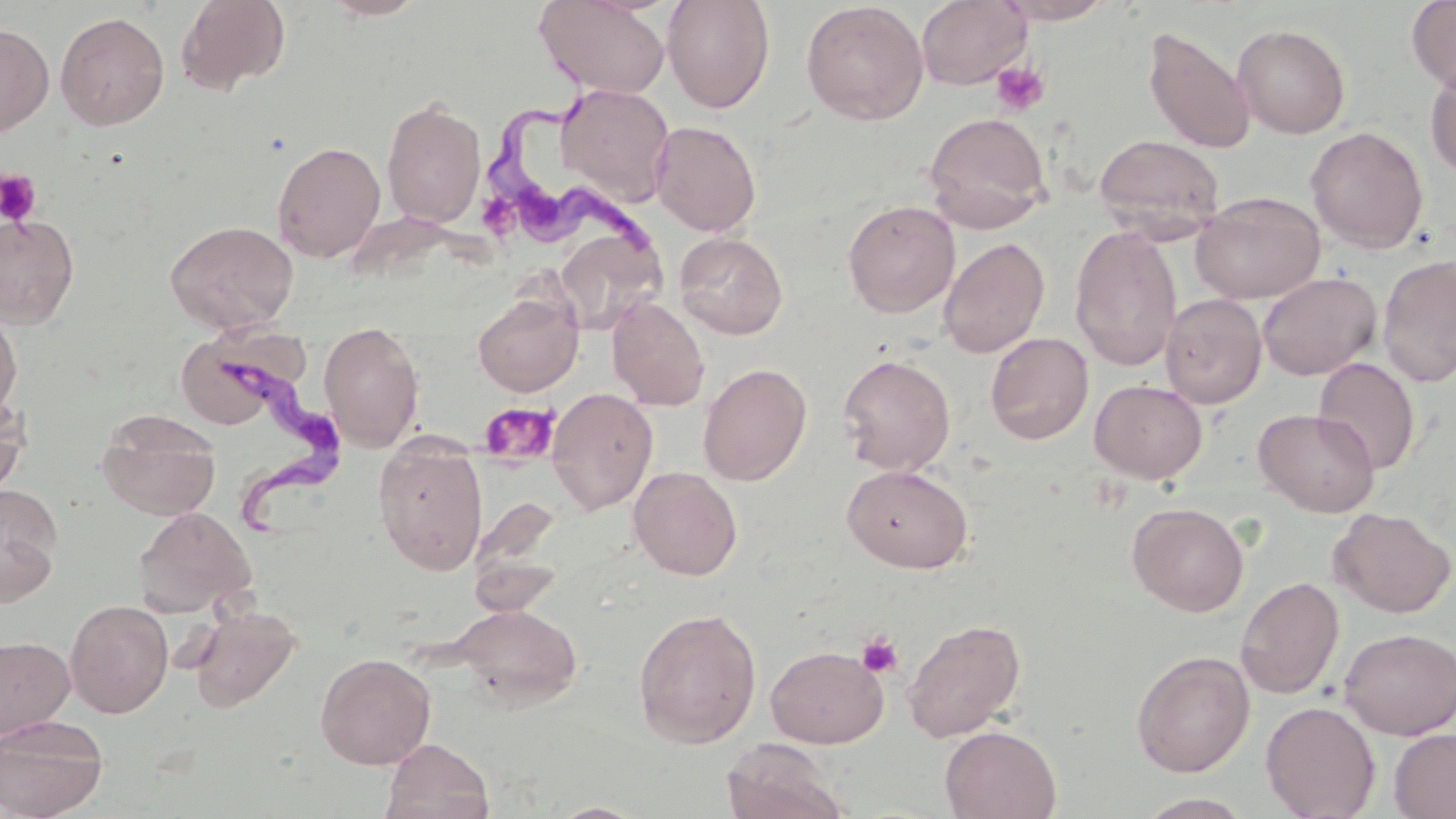

Summary:
  - Coordinate format: approximate bounding boxes as [x1, y1, x2, y2] in pixels
  - Uninfected red blood cell locations: [174, 0, 291, 95], [321, 0, 429, 20], [535, 0, 671, 99], [661, 0, 776, 113], [916, 0, 1031, 89], [994, 0, 1117, 24], [1406, 0, 1456, 94], [801, 1, 929, 125], [54, 11, 170, 131], [0, 23, 54, 137], [1231, 23, 1351, 139], [1142, 25, 1256, 155], [1425, 63, 1456, 178], [556, 83, 675, 206], [381, 97, 487, 229], [922, 111, 1052, 233], [650, 120, 761, 236], [1305, 126, 1429, 253], [1092, 133, 1225, 241], [271, 140, 386, 262], [1190, 191, 1325, 304], [843, 200, 960, 318], [0, 213, 79, 329], [164, 220, 299, 334], [553, 224, 666, 334], [1069, 225, 1182, 371], [674, 231, 788, 340], [938, 237, 1050, 358], [1377, 253, 1456, 388], [1257, 271, 1382, 381], [472, 292, 583, 396], [1160, 293, 1267, 408], [607, 297, 710, 411], [0, 307, 22, 423], [319, 320, 424, 452], [174, 325, 316, 422], [985, 332, 1094, 445], [837, 353, 956, 475], [1313, 357, 1420, 475], [698, 363, 812, 485], [1090, 379, 1207, 484], [546, 387, 658, 515], [0, 391, 28, 496], [1253, 408, 1380, 517], [96, 409, 221, 520], [373, 438, 488, 575], [842, 464, 974, 573], [628, 466, 743, 580], [0, 483, 63, 604], [469, 493, 568, 610], [1127, 502, 1249, 616], [133, 506, 256, 617], [1328, 507, 1455, 618], [1235, 577, 1344, 699], [65, 598, 173, 718], [189, 604, 301, 713], [451, 604, 583, 709], [632, 607, 762, 748], [902, 618, 1026, 742], [1338, 627, 1456, 739], [0, 635, 75, 738], [765, 644, 889, 748], [1131, 650, 1254, 777], [315, 652, 436, 769], [1261, 701, 1380, 819], [0, 714, 109, 818], [940, 725, 1062, 819], [1388, 727, 1456, 818], [380, 738, 494, 819], [720, 739, 850, 819], [1133, 792, 1258, 818], [547, 801, 649, 819]
  - Platelet locations: [990, 61, 1050, 116], [0, 169, 41, 227], [477, 191, 524, 246], [478, 401, 559, 466], [857, 632, 903, 678]
  - Trypanosoma brucei locations: [483, 70, 665, 266], [212, 345, 349, 540]
  - Slide-level diagnosis: Trypanosoma brucei
  - Preparation: thin blood film
  - Modality: light microscopy
  - Magnification: 1000x
  - Field of view: one of a larger specimen
  - Stain: May-Grünwald-Giemsa
  - Image size: 1456×819 pixels